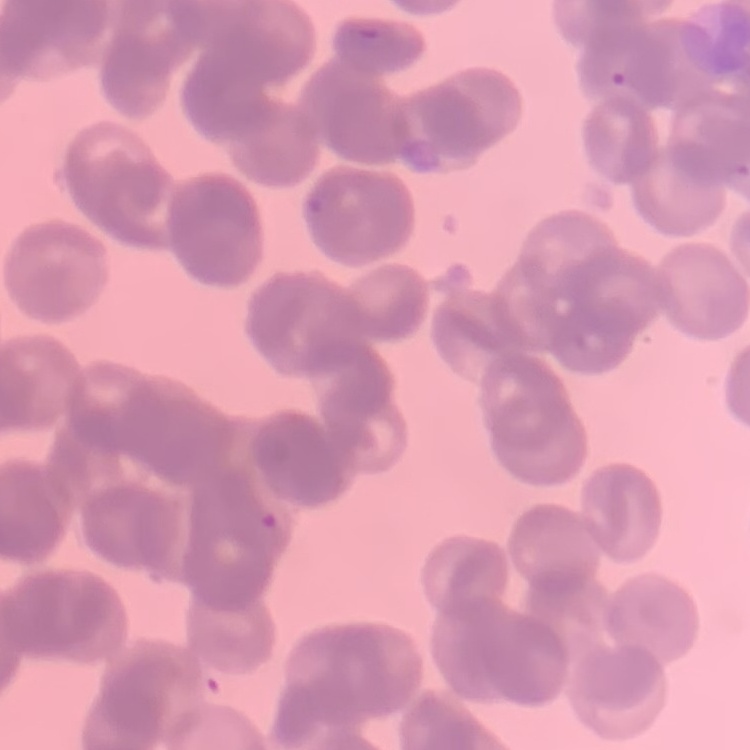

red blood cell morphology = rouleaux formation
stain = Field's or Giemsa
preparation = thin blood film
image type = square crop of a larger photomicrograph